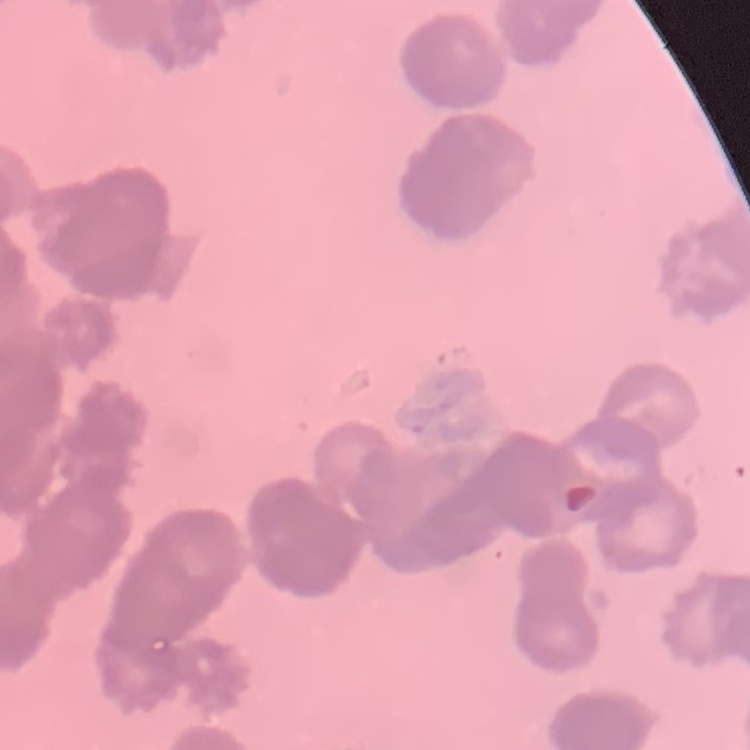

The erythrocytes exhibit rouleaux formation. Stained with either Field's or Giemsa. Thin blood smear. Square crop of a larger photomicrograph.